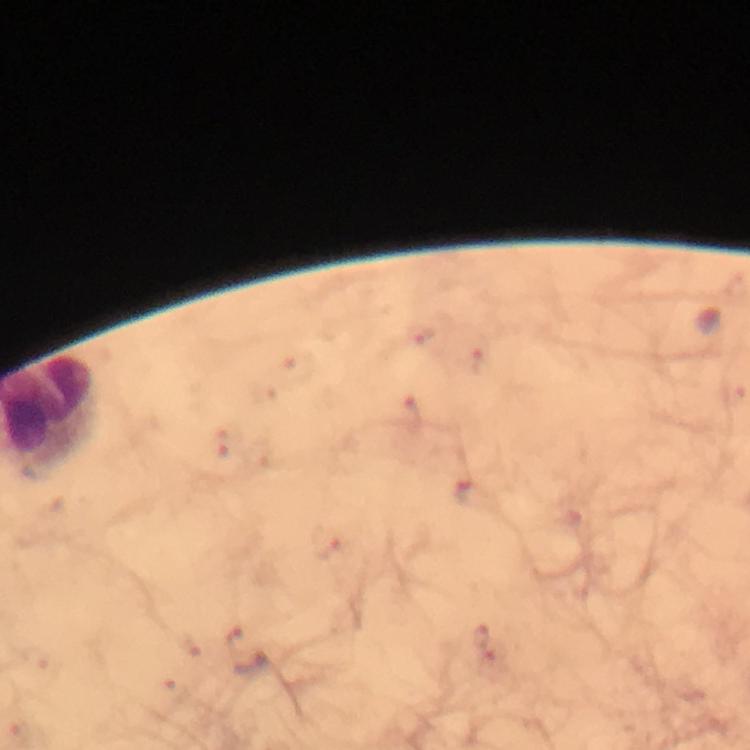
Approximate object centers, in pixels from the top-left corner. Plasmodium parasite locations: (x=418, y=335), (x=480, y=363), (x=412, y=413), (x=222, y=445), (x=469, y=492), (x=327, y=544), (x=480, y=634), (x=235, y=639), (x=493, y=656). Giemsa-stained preparation. Cropped region of a single field of view. Thick blood smear. From a malaria diagnostic workup. Photographed with a smartphone mounted on the microscope. Image is 750×750 pixels. Immersion oil was used. 100x magnification.